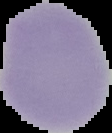

Summary:
  - Image size: 112×133 pixels
  - Result: negative for Plasmodium parasites
  - Preparation: thin blood smear
  - Image type: segmented cell region with the area outside set to black